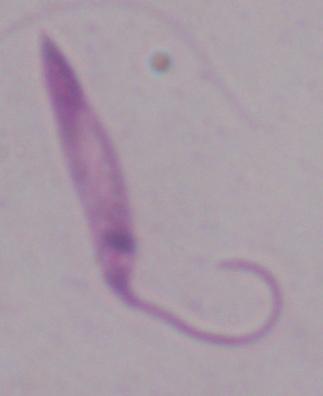
{
  "identification": "Leishmania",
  "magnification": "1000x",
  "modality": "micrograph"
}